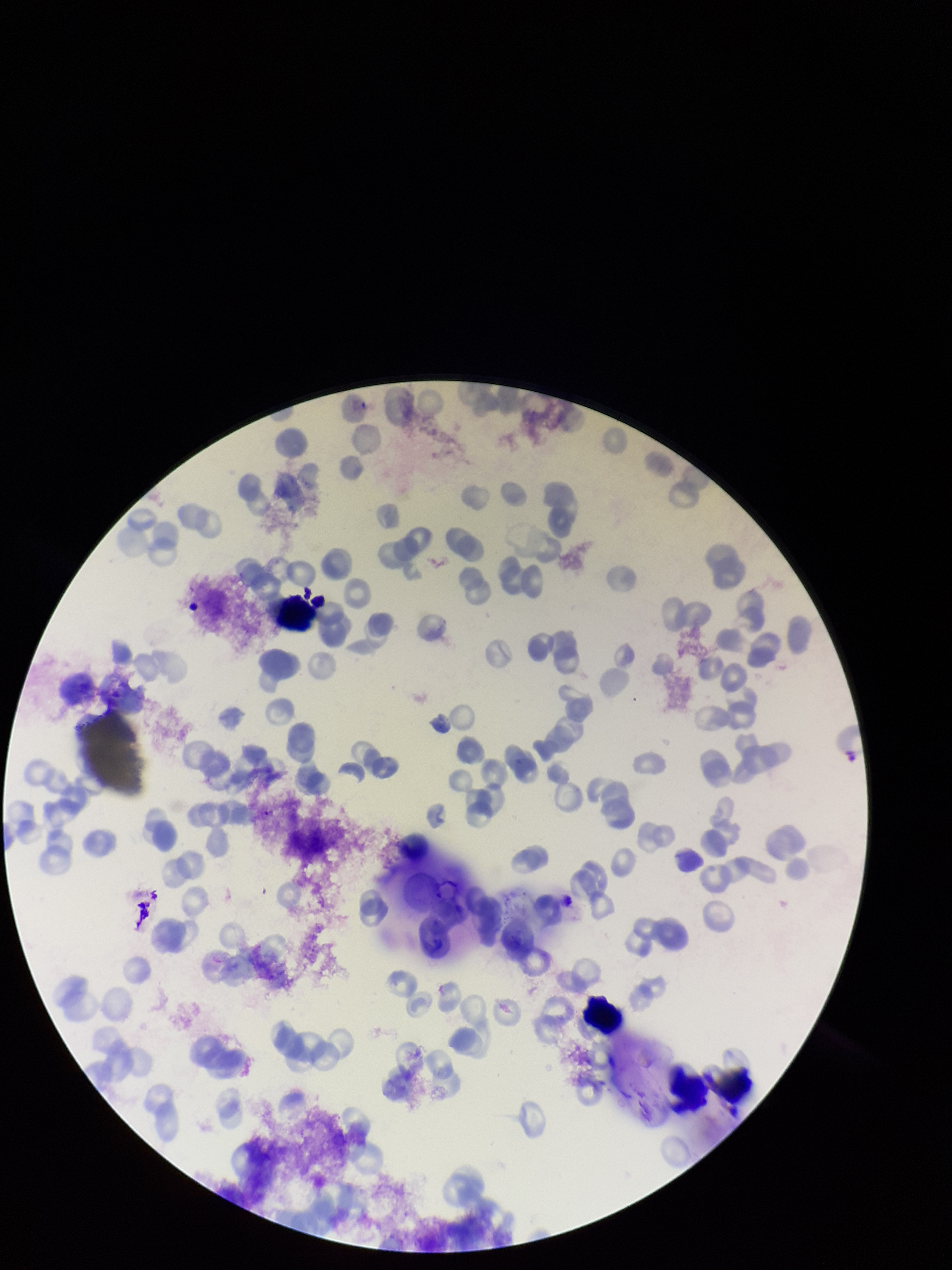
field_of_view: one from this slide
parasitized_red_blood_cells: none identified
red_blood_cell_count: 117
capture: smartphone photograph through the microscope eyepiece
species_reported_for_this_patient: Plasmodium vivax
patient_malaria_status: positive
image_size: 952×1270 pixels
preparation: thin blood smear
stain: Giemsa
parasitized_red_blood_cell_count: 0